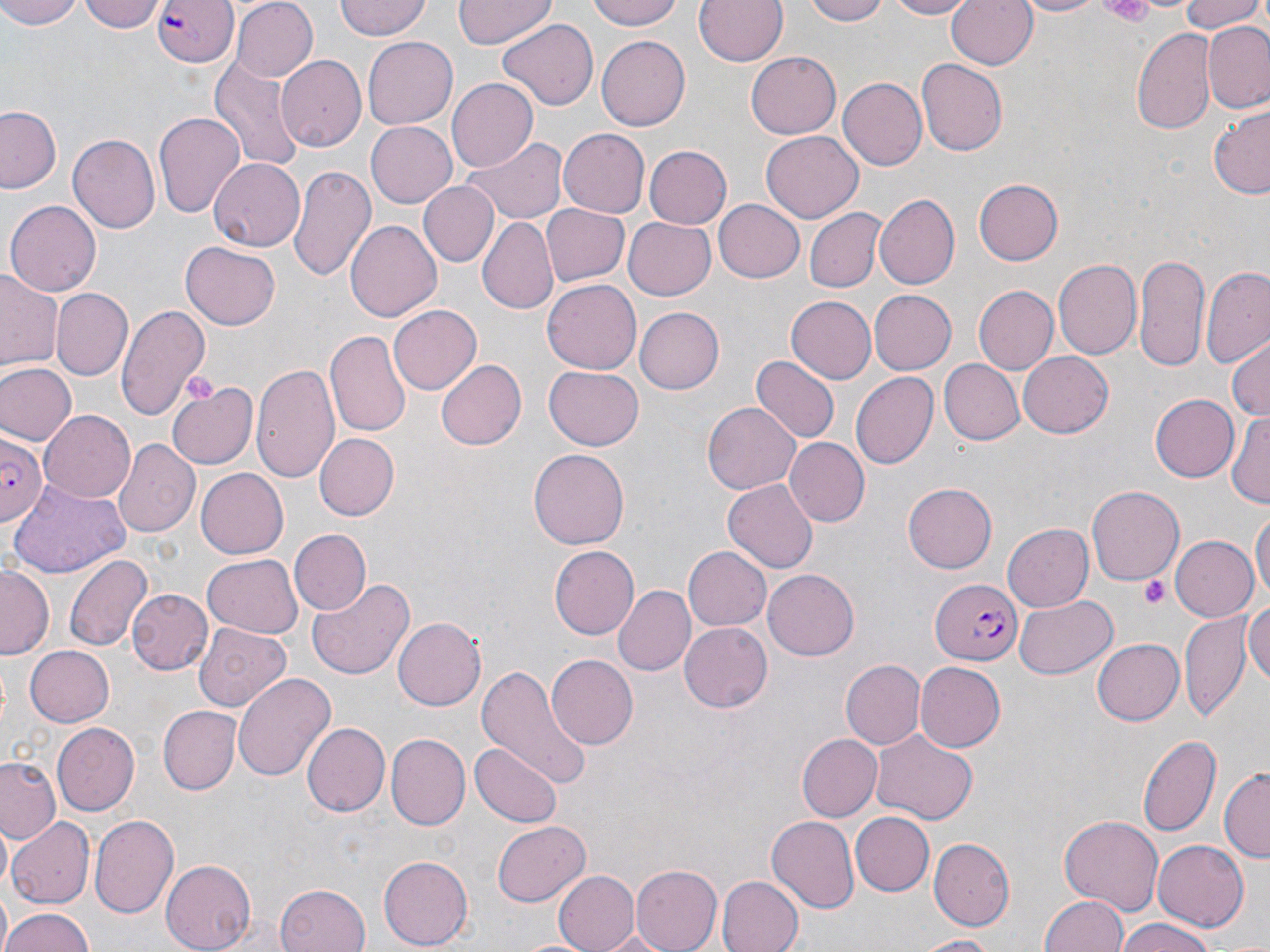 Approximate bounding boxes as (x1, y1, x2, y2) in pixels. Platelet locations: (1087, 0, 1160, 24), (1140, 575, 1170, 608). Plasmodium falciparum-infected red blood cell locations: (154, 0, 240, 69), (0, 432, 48, 524), (929, 578, 1020, 662). Uninfected red blood cell locations: (0, 0, 88, 29), (80, 0, 164, 34), (332, 0, 432, 41), (452, 0, 554, 50), (588, 0, 686, 30), (695, 0, 787, 67), (803, 0, 893, 25), (880, 0, 980, 19), (946, 0, 1038, 73), (1012, 0, 1105, 18), (1174, 0, 1265, 33), (230, 1, 319, 82), (497, 20, 598, 111), (1203, 23, 1270, 112), (1132, 29, 1215, 133), (597, 35, 690, 130), (360, 37, 457, 129), (747, 51, 841, 141), (280, 56, 367, 152), (210, 57, 303, 169), (915, 59, 1007, 156), (836, 78, 926, 171), (448, 79, 539, 171), (0, 105, 63, 194), (1210, 108, 1270, 199), (154, 112, 246, 220), (365, 120, 459, 207), (559, 130, 649, 215), (761, 132, 863, 221), (69, 134, 160, 237), (463, 137, 568, 224), (644, 145, 732, 230), (209, 159, 305, 252), (290, 164, 375, 284), (972, 176, 1063, 266), (418, 181, 499, 267), (874, 194, 960, 290), (4, 199, 101, 296), (715, 200, 804, 282), (540, 204, 629, 287), (804, 206, 884, 292), (478, 216, 557, 315), (623, 217, 717, 301), (345, 220, 441, 322), (180, 241, 281, 329), (1134, 252, 1209, 371), (1055, 258, 1143, 360), (1200, 267, 1270, 369), (0, 273, 61, 374), (544, 279, 640, 373), (974, 286, 1060, 374), (868, 288, 955, 373), (51, 290, 131, 380), (785, 296, 876, 385), (114, 303, 209, 420), (389, 303, 482, 393), (635, 306, 725, 393), (325, 330, 410, 438), (1228, 336, 1270, 423), (1018, 352, 1114, 438), (753, 355, 837, 443), (938, 358, 1022, 445), (436, 359, 526, 450), (1, 362, 76, 446), (251, 362, 341, 487), (545, 365, 644, 449), (850, 371, 939, 470), (166, 382, 257, 471), (1152, 393, 1238, 481), (703, 403, 800, 494), (1226, 407, 1270, 506), (39, 410, 136, 503), (313, 432, 398, 520), (786, 436, 870, 525), (114, 440, 199, 538), (529, 448, 630, 549), (197, 469, 288, 558), (723, 478, 817, 572), (902, 484, 997, 574), (1087, 485, 1184, 586), (1251, 508, 1269, 604), (1003, 523, 1092, 612), (287, 529, 369, 615), (1169, 535, 1259, 622), (549, 543, 638, 640), (684, 545, 771, 631), (66, 552, 150, 653), (201, 555, 302, 637), (0, 566, 52, 657), (762, 569, 859, 661), (306, 575, 412, 681), (615, 584, 694, 677), (126, 590, 211, 675), (1015, 594, 1118, 679), (1245, 598, 1270, 690), (1180, 612, 1251, 722), (392, 617, 484, 711), (193, 621, 295, 713), (679, 621, 771, 713), (1090, 638, 1182, 727), (25, 645, 116, 726), (546, 655, 637, 750), (841, 659, 924, 749), (914, 662, 1006, 753), (474, 664, 593, 790), (232, 672, 335, 785), (158, 706, 239, 794), (51, 721, 139, 816), (301, 722, 390, 818), (869, 728, 979, 824), (1136, 733, 1220, 839), (387, 734, 471, 831), (795, 734, 880, 821), (472, 742, 560, 825), (0, 756, 62, 841), (1219, 768, 1270, 863), (90, 812, 180, 921), (850, 812, 934, 895), (1059, 815, 1164, 917), (768, 816, 859, 911), (9, 817, 95, 908), (492, 821, 589, 908), (929, 837, 1016, 929), (1151, 839, 1248, 932), (377, 857, 470, 950), (161, 859, 258, 950), (630, 865, 722, 952), (551, 869, 639, 952), (718, 875, 803, 952), (275, 884, 370, 952), (1040, 892, 1132, 952), (0, 908, 96, 952), (1112, 919, 1223, 952), (912, 934, 1006, 951). Slide-level diagnosis: Plasmodium falciparum. 1000x magnification. May-Grünwald-Giemsa-stained preparation. Single field of view. Thin blood smear. Image is 1270×952 pixels. Light microscopy.